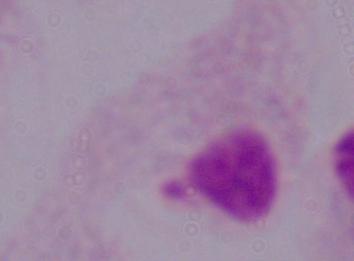
Summary:
  - Modality: micrograph
  - Magnification: 1000x
  - Identification: trichomonad